Classify this cell by malaria status.
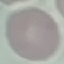

It is uninfected.

Summary:
  - Stain: Giemsa
  - Image type: cell patch, automatically extracted from a larger field of view and resized to 64 × 64 pixels
  - Capture: smartphone camera at the microscope eyepiece
  - Preparation: thin blood smear